Assess for malaria.
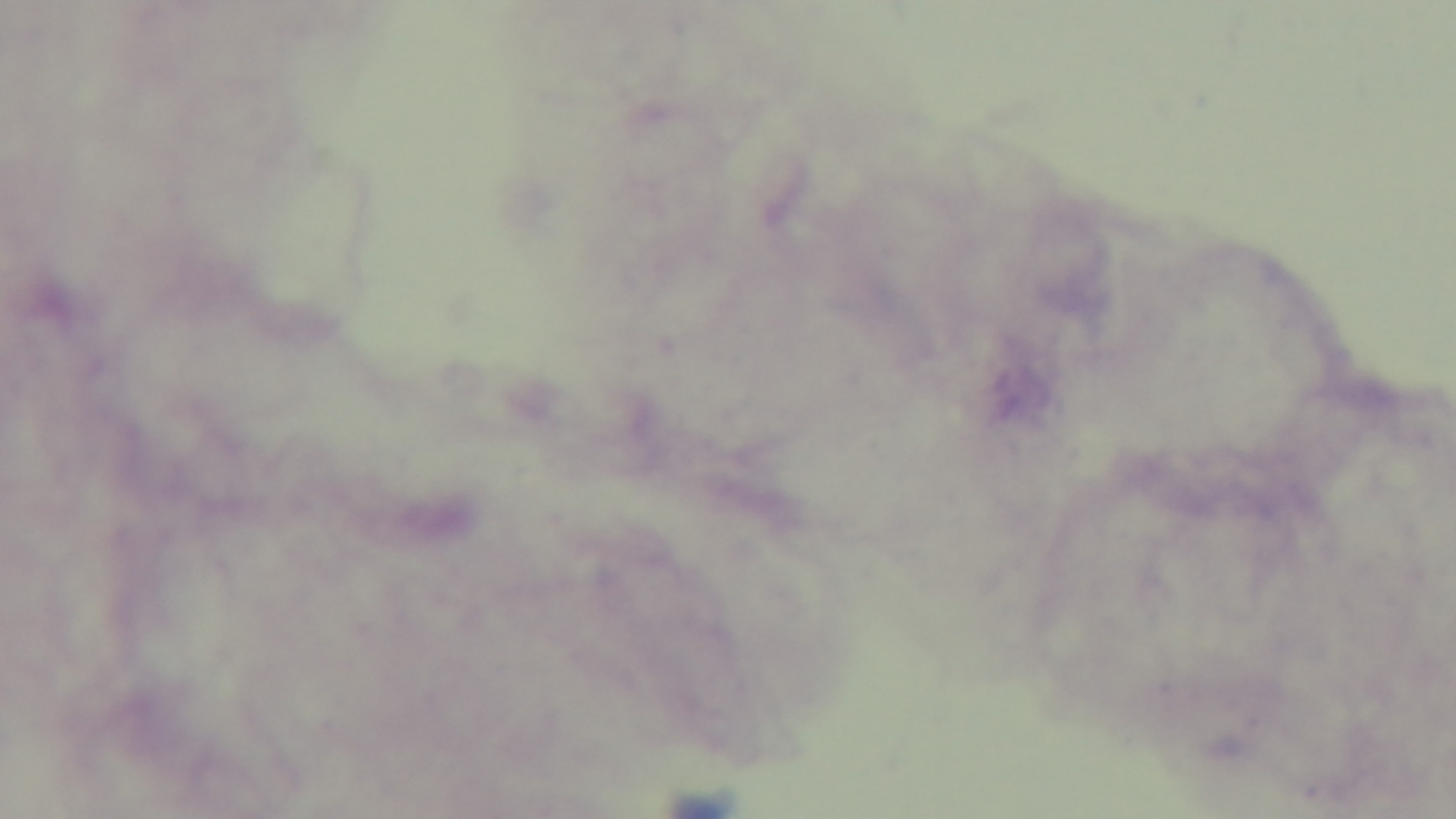

It is uninfected.

preparation: thick blood film
capture: mounted 4K digital camera
modality: light microscopy
stain: Giemsa
objective: 100x oil immersion
field_of_view: one from the slide